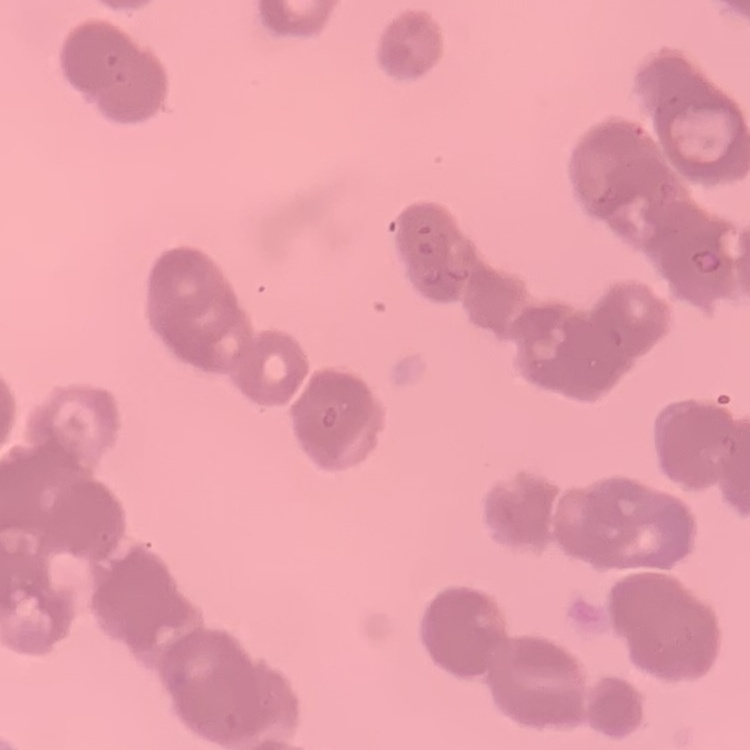
Summary:
  - Red blood cell morphology: rouleaux formation
  - Image type: one tile cut from a larger photomicrograph
  - Preparation: thin blood film
  - Stain: Field's or Giemsa